Locate and identify every blood parasite.
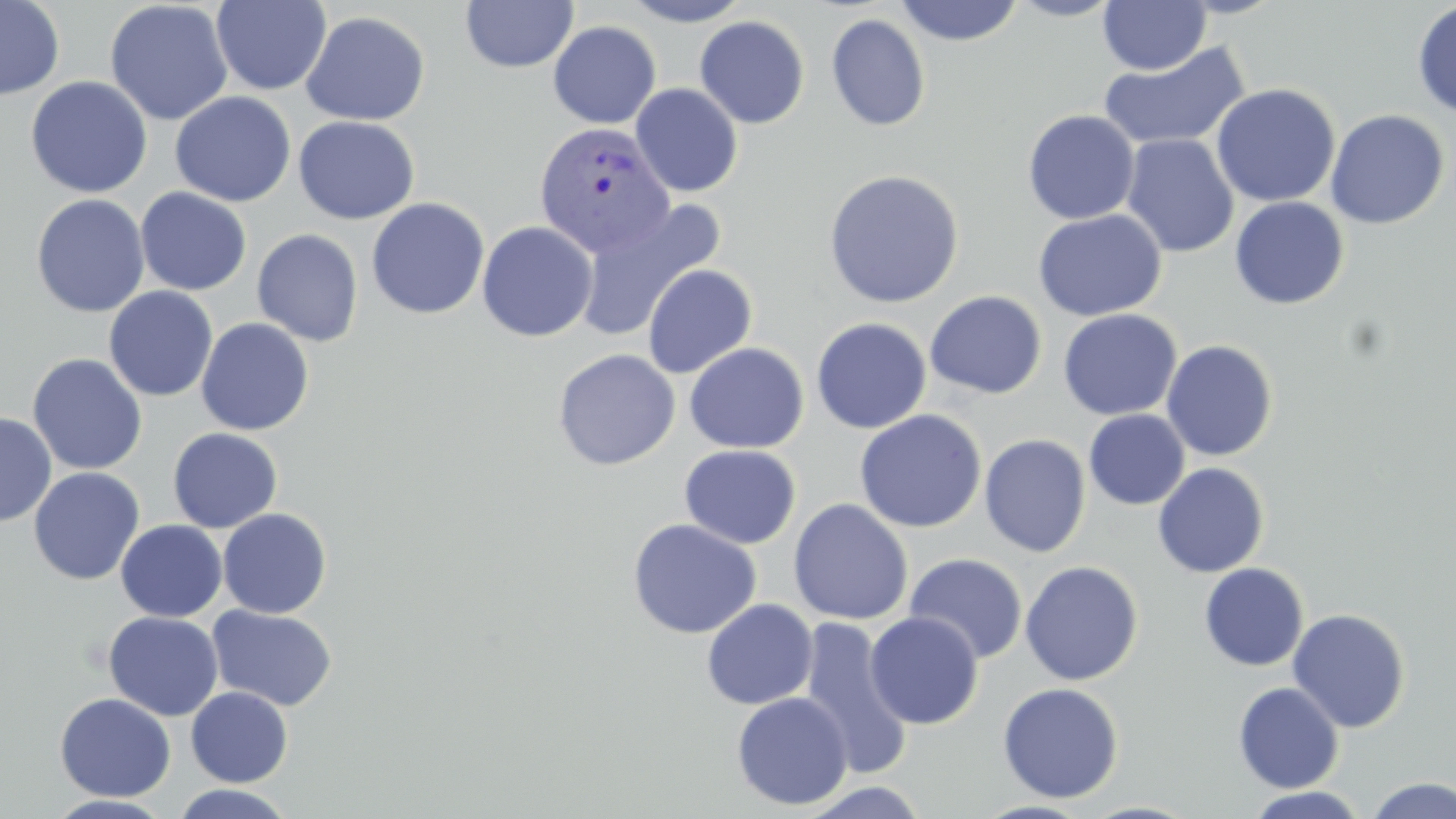
Approximate bounding boxes as named x1/y1/x2/y2 corners in pixels.
Plasmodium vivax-infected red blood cells: (x1=533, y1=121, x2=676, y2=258).
No Plasmodium falciparum, Plasmodium ovale, Plasmodium malariae, Babesia divergens, or Trypanosoma brucei observed.

Uninfected red blood cell locations: (x1=0, y1=0, x2=65, y2=101), (x1=461, y1=0, x2=579, y2=74), (x1=620, y1=0, x2=755, y2=26), (x1=893, y1=0, x2=1024, y2=46), (x1=1007, y1=0, x2=1123, y2=21), (x1=1097, y1=0, x2=1211, y2=75), (x1=1175, y1=0, x2=1286, y2=19), (x1=211, y1=1, x2=331, y2=95), (x1=104, y1=2, x2=233, y2=125), (x1=1411, y1=3, x2=1456, y2=119), (x1=300, y1=11, x2=430, y2=126), (x1=826, y1=13, x2=931, y2=132), (x1=694, y1=15, x2=810, y2=129), (x1=548, y1=21, x2=662, y2=129), (x1=1098, y1=41, x2=1252, y2=152), (x1=25, y1=76, x2=153, y2=198), (x1=630, y1=83, x2=744, y2=197), (x1=1211, y1=83, x2=1340, y2=208), (x1=170, y1=92, x2=297, y2=207), (x1=1022, y1=109, x2=1140, y2=225), (x1=1324, y1=109, x2=1449, y2=229), (x1=293, y1=115, x2=420, y2=225), (x1=1120, y1=134, x2=1239, y2=258), (x1=823, y1=168, x2=965, y2=309), (x1=135, y1=188, x2=252, y2=295), (x1=30, y1=194, x2=150, y2=318), (x1=573, y1=197, x2=727, y2=343), (x1=1229, y1=197, x2=1349, y2=309), (x1=366, y1=198, x2=490, y2=320), (x1=1033, y1=209, x2=1167, y2=321), (x1=477, y1=221, x2=598, y2=342), (x1=252, y1=229, x2=364, y2=347), (x1=641, y1=263, x2=758, y2=378), (x1=103, y1=286, x2=218, y2=402), (x1=925, y1=290, x2=1047, y2=399), (x1=1058, y1=308, x2=1182, y2=420), (x1=195, y1=317, x2=314, y2=436), (x1=811, y1=317, x2=932, y2=433), (x1=1161, y1=339, x2=1278, y2=461), (x1=683, y1=342, x2=809, y2=453), (x1=553, y1=349, x2=680, y2=471), (x1=27, y1=353, x2=148, y2=475), (x1=854, y1=409, x2=987, y2=533), (x1=1084, y1=409, x2=1190, y2=510), (x1=0, y1=412, x2=57, y2=527), (x1=167, y1=427, x2=283, y2=533), (x1=979, y1=433, x2=1091, y2=557), (x1=679, y1=444, x2=801, y2=549), (x1=1153, y1=462, x2=1269, y2=577), (x1=28, y1=467, x2=145, y2=586), (x1=789, y1=498, x2=913, y2=625), (x1=217, y1=508, x2=332, y2=619), (x1=626, y1=518, x2=762, y2=639), (x1=116, y1=520, x2=227, y2=621), (x1=904, y1=553, x2=1028, y2=664), (x1=1020, y1=561, x2=1143, y2=686), (x1=1199, y1=563, x2=1308, y2=671), (x1=701, y1=598, x2=818, y2=710), (x1=207, y1=605, x2=337, y2=712), (x1=1287, y1=608, x2=1411, y2=733), (x1=103, y1=610, x2=224, y2=721), (x1=864, y1=611, x2=984, y2=729), (x1=798, y1=616, x2=913, y2=779), (x1=997, y1=681, x2=1125, y2=804), (x1=1233, y1=681, x2=1344, y2=793), (x1=186, y1=686, x2=293, y2=787), (x1=731, y1=691, x2=853, y2=811), (x1=54, y1=692, x2=176, y2=802), (x1=1364, y1=776, x2=1455, y2=819), (x1=798, y1=781, x2=933, y2=819), (x1=168, y1=784, x2=296, y2=819), (x1=1244, y1=786, x2=1369, y2=818), (x1=45, y1=794, x2=175, y2=818). Slide-level diagnosis: Plasmodium vivax. Captured at 1000x magnification. Optical microscopy. May-Grünwald-Giemsa-stained preparation. Image is 1456×819 pixels. Thin blood smear. Single field of view.